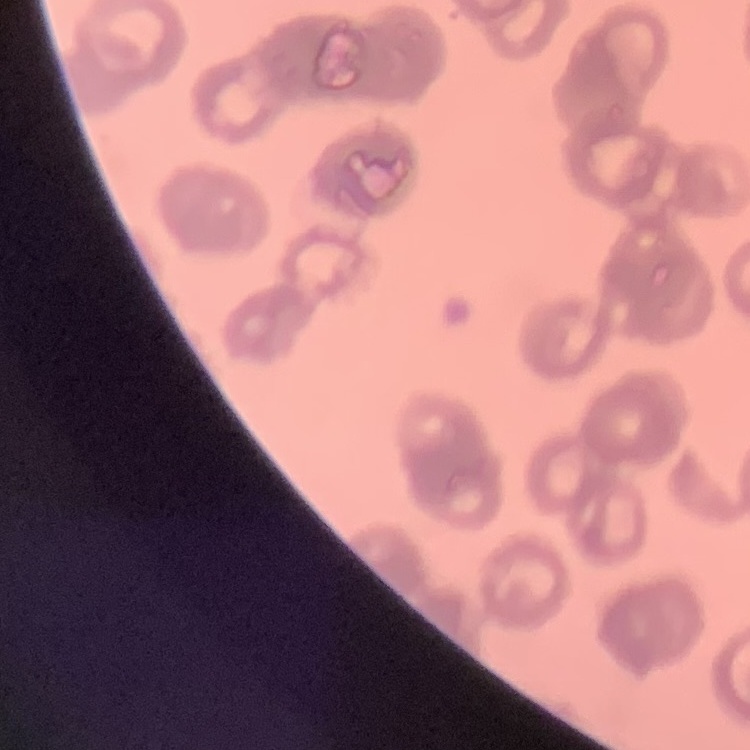

The red blood cells exhibit rouleaux formation. Thin blood smear. One tile cut from a larger photomicrograph. Stained with either Field's or Giemsa.